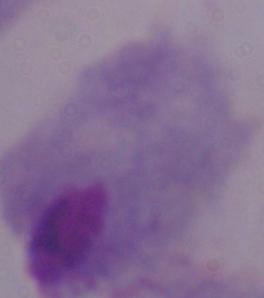 A trichomonad is seen. Captured at 1000x magnification. Micrograph.